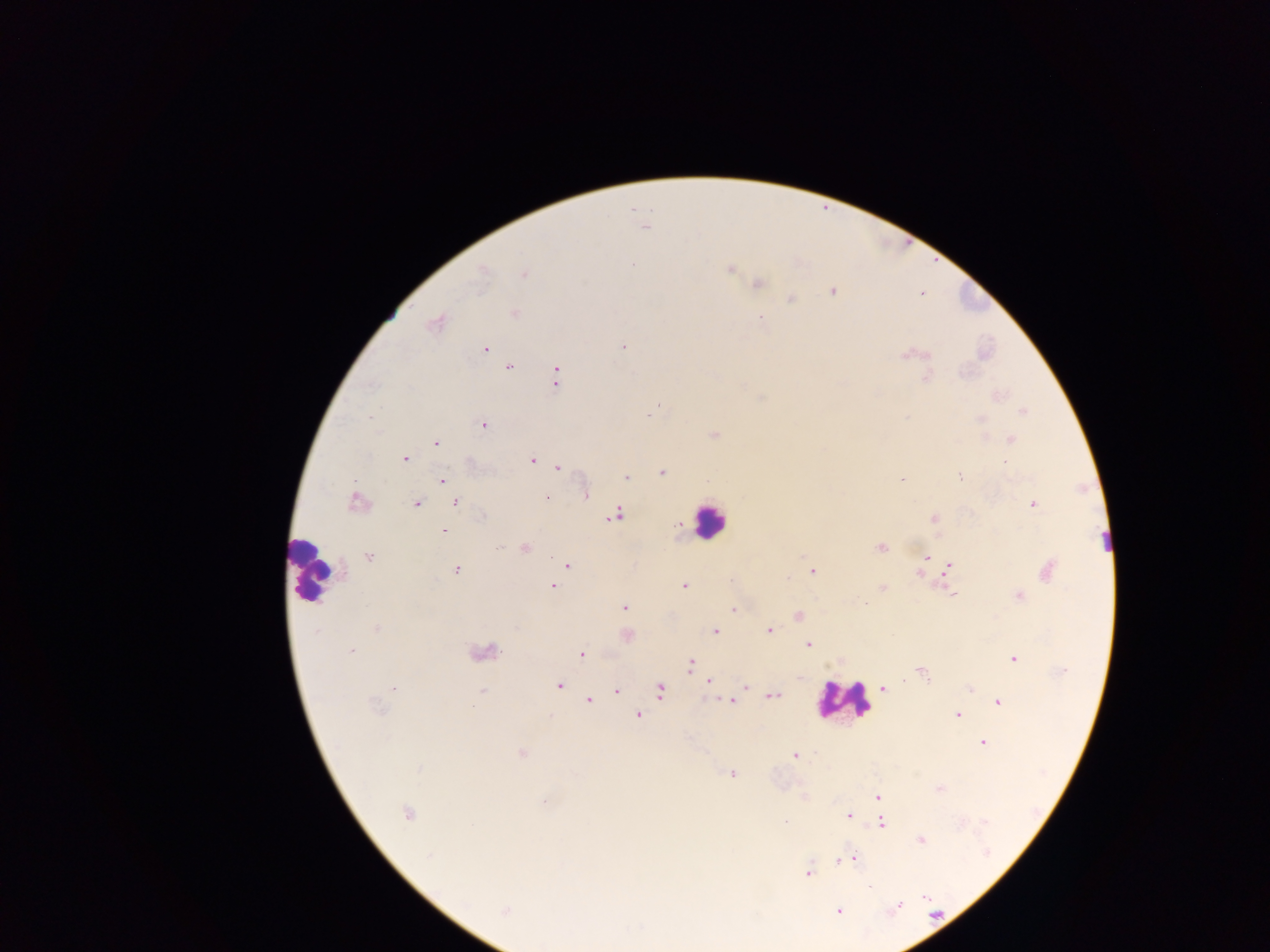

Approximate centers as [x, y] in pixels.
Summary:
  - Plasmodium parasite locations: [645, 227], [632, 265], [729, 267], [481, 269], [524, 274], [757, 284], [833, 290], [921, 292], [790, 298], [514, 313], [436, 321], [623, 346], [485, 348], [912, 355], [508, 367], [556, 375], [926, 376], [996, 395], [1022, 410], [648, 414], [980, 419], [483, 424], [714, 435], [1011, 439], [435, 443], [404, 459], [532, 460], [554, 464], [558, 467], [662, 471], [960, 477], [625, 478], [442, 479], [901, 479], [585, 492], [547, 498], [356, 501], [456, 502], [1032, 503], [415, 504], [615, 513], [933, 518], [679, 525], [444, 531], [524, 548], [880, 548], [368, 557], [927, 557], [567, 565], [948, 567], [455, 569], [1046, 569], [812, 571], [920, 575], [684, 585], [552, 586], [881, 588], [951, 593], [1019, 596], [624, 607], [733, 609], [798, 615], [375, 629], [715, 630], [768, 631], [625, 635], [807, 644], [350, 651], [482, 652], [581, 654], [1013, 659], [690, 664], [921, 670], [709, 680], [560, 684], [743, 684], [393, 688], [883, 688], [972, 689], [660, 690], [617, 691], [482, 692], [771, 695], [589, 700], [732, 700], [998, 701], [377, 709], [638, 715], [957, 715], [982, 742], [521, 753], [795, 756], [731, 773], [939, 788], [877, 796], [805, 798], [407, 813], [848, 815], [880, 822], [921, 839], [852, 858], [837, 861], [807, 872], [505, 910], [837, 910]
  - Leukocyte locations: [709, 520], [311, 573], [843, 700]
  - Field of view: single
  - Capture: mobile-phone photograph through a microscope
  - Image size: 1270×952 pixels
  - Country: Ghana
  - Preparation: thick blood film